Look for Plasmodium parasites.
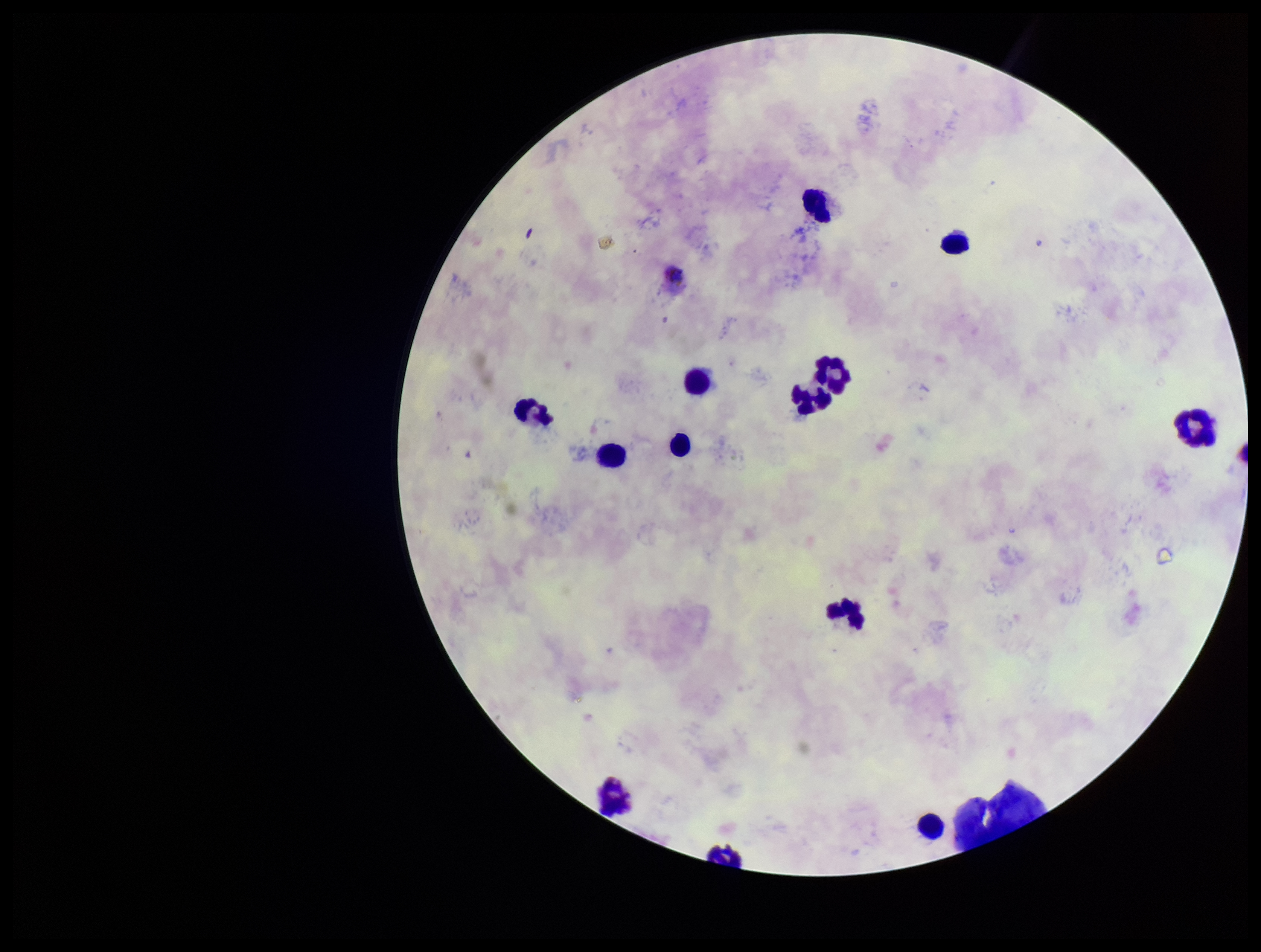
None seen.

Summary:
  - Field of view: one from this slide
  - Image size: 1261×952 pixels
  - Leukocyte count: 14
  - Stain: Giemsa
  - Species reported for this patient: Plasmodium vivax
  - Parasite count: 0
  - Patient malaria status: infected
  - Preparation: thick blood smear
  - Capture: smartphone photograph through the microscope eyepiece